Identify the blood parasite species.
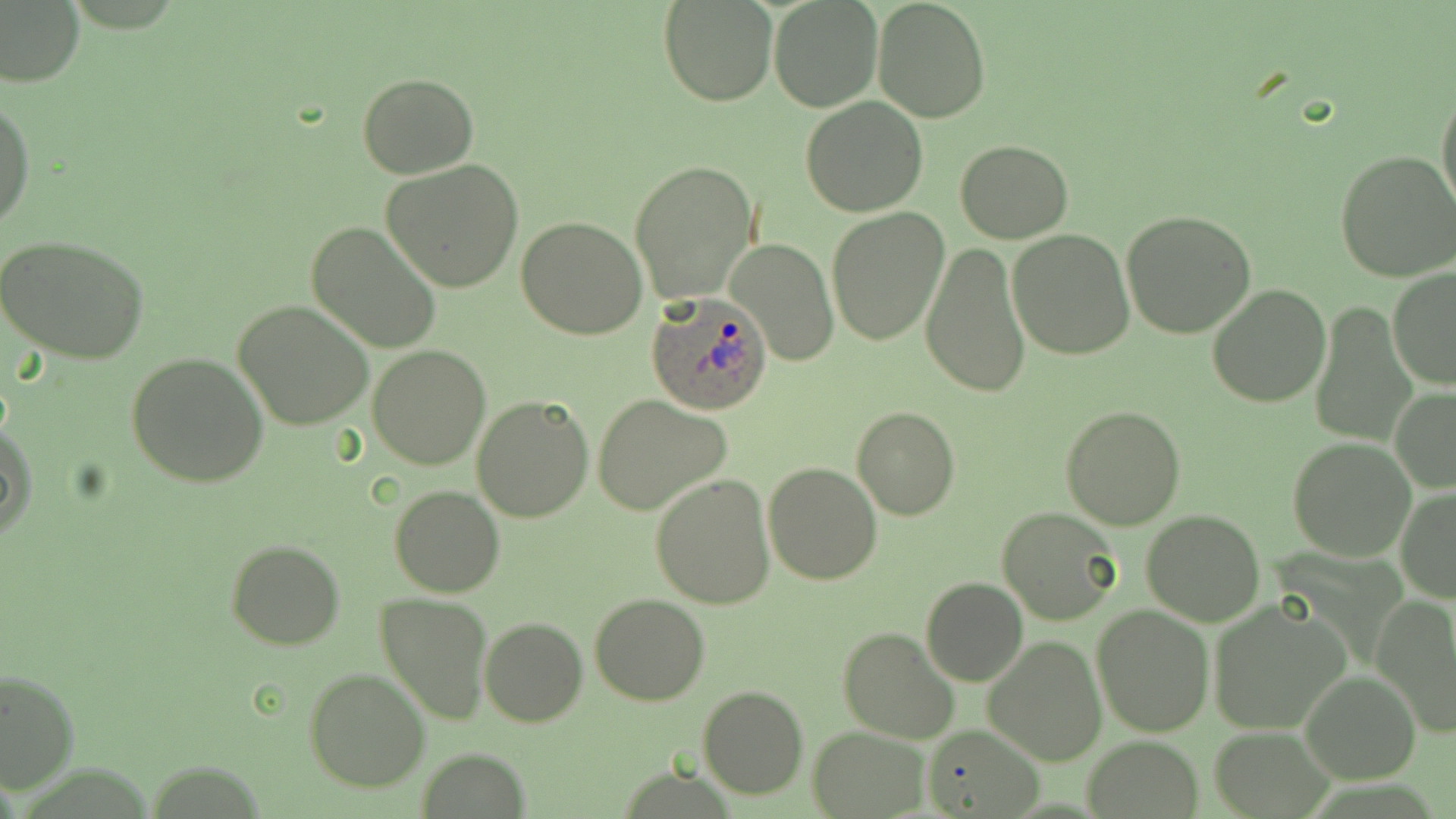

Plasmodium ovale.

Summary:
  - Coordinate format: approximate bounding boxes as (x1,y1)-(x2,y2) corner pairs in pixels
  - Plasmodium ovale-infected red blood cell locations: (646,291)-(773,416)
  - Uninfected red blood cell locations: (0,0)-(85,89), (872,0)-(991,124), (658,1)-(777,105), (769,1)-(882,112), (357,72)-(479,179), (1436,82)-(1456,222), (0,96)-(35,232), (800,96)-(929,218), (954,140)-(1073,243), (1336,150)-(1456,282), (380,160)-(524,294), (630,160)-(759,304), (826,208)-(949,345), (1122,210)-(1258,338), (516,217)-(647,339), (307,221)-(440,355), (1007,229)-(1135,360), (0,233)-(151,364), (727,238)-(839,366), (920,243)-(1033,399), (1388,266)-(1456,391), (1207,283)-(1330,408), (234,300)-(375,430), (1311,301)-(1415,445), (368,344)-(490,469), (125,351)-(270,488), (1390,386)-(1456,494), (591,394)-(732,515), (471,395)-(595,524), (852,405)-(960,521), (1060,406)-(1187,530), (1,421)-(36,542), (1286,436)-(1417,560), (762,461)-(884,585), (650,474)-(778,608), (389,485)-(505,597), (1396,486)-(1456,601), (997,507)-(1123,627), (1140,509)-(1266,627), (226,540)-(345,651), (920,578)-(1028,687), (375,593)-(493,726), (589,594)-(710,706), (1372,595)-(1456,738), (1206,600)-(1348,734), (1092,604)-(1214,736), (479,617)-(588,727), (838,627)-(962,746), (982,634)-(1108,767), (0,667)-(79,793), (303,668)-(430,792), (1300,670)-(1419,783), (698,686)-(808,801), (922,725)-(1045,818), (807,726)-(928,818), (1207,726)-(1333,816), (1084,737)-(1203,816), (416,747)-(530,818)
  - Field of view: single
  - Image size: 1456×819 pixels
  - Modality: light microscopy
  - Stain: May-Grünwald-Giemsa
  - Preparation: thin blood smear
  - Magnification: 1000x